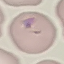
malaria status = parasitized
image type = cell patch, automatically extracted from a larger field of view and resized to 64 × 64 pixels
capture = smartphone through the microscope eyepiece
preparation = thin blood film
stain = Giemsa